Give the location of every parasitized RBC.
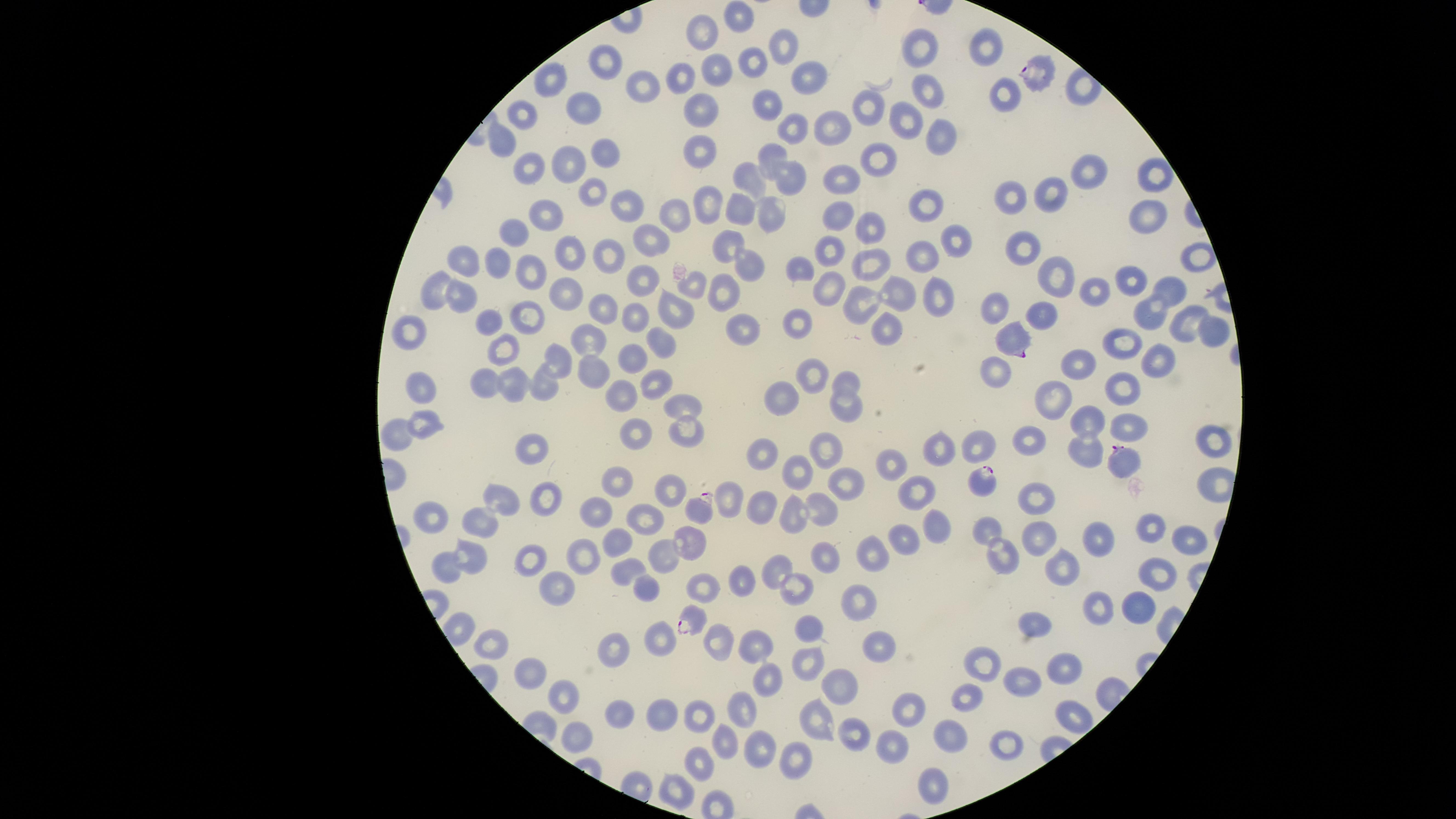

Approximate marker points as {x, y} in pixels.
Parasitized RBCs: {1035, 69}, {1015, 334}, {1123, 460}, {979, 476}, {699, 508}, {693, 619}.

Approximate marker points as {x, y} in pixels. Uninfected RBCs: {737, 18}, {703, 34}, {779, 46}, {923, 48}, {987, 48}, {604, 62}, {750, 67}, {717, 69}, {685, 77}, {547, 78}, {808, 78}, {644, 86}, {928, 88}, {1003, 97}, {765, 105}, {584, 107}, {868, 108}, {703, 109}, {520, 117}, {907, 118}, {792, 127}, {834, 129}, {941, 133}, {506, 142}, {698, 146}, {606, 149}, {775, 157}, {883, 159}, {574, 164}, {529, 168}, {1090, 173}, {1151, 174}, {793, 175}, {748, 178}, {841, 181}, {592, 190}, {1052, 190}, {1011, 200}, {711, 204}, {930, 204}, {628, 206}, {742, 212}, {835, 213}, {549, 214}, {678, 216}, {771, 216}, {1148, 216}, {517, 225}, {868, 227}, {650, 237}, {953, 238}, {727, 244}, {829, 250}, {1021, 250}, {922, 254}, {569, 256}, {607, 257}, {1197, 257}, {468, 260}, {743, 261}, {870, 261}, {502, 264}, {530, 271}, {798, 272}, {1056, 272}, {1128, 278}, {640, 281}, {691, 285}, {726, 289}, {826, 291}, {1168, 291}, {438, 292}, {567, 292}, {901, 292}, {1094, 292}, {938, 296}, {462, 299}, {860, 301}, {597, 306}, {996, 308}, {680, 310}, {1150, 314}, {632, 315}, {529, 317}, {1043, 319}, {886, 321}, {487, 323}, {799, 323}, {1180, 324}, {743, 327}, {413, 330}, {1209, 331}, {589, 337}, {663, 337}, {1120, 343}, {507, 350}, {558, 358}, {635, 360}, {1079, 362}, {1161, 363}, {593, 370}, {994, 375}, {810, 376}, {661, 384}, {848, 384}, {490, 385}, {544, 385}, {1121, 386}, {419, 387}, {522, 387}, {625, 391}, {1056, 396}, {781, 397}, {847, 404}, {691, 409}, {1089, 419}, {425, 425}, {1132, 425}, {633, 427}, {401, 432}, {684, 433}, {1212, 437}, {1032, 440}, {981, 441}, {538, 445}, {826, 447}, {943, 447}, {1082, 448}, {767, 453}, {893, 463}, {796, 468}, {616, 484}, {847, 485}, {667, 488}, {916, 494}, {544, 497}, {1037, 497}, {501, 498}, {729, 499}, {760, 503}, {824, 508}, {599, 510}, {431, 517}, {644, 517}, {789, 517}, {484, 525}, {936, 525}, {991, 527}, {1149, 528}, {1038, 535}, {903, 537}, {619, 540}, {691, 540}, {1186, 540}, {1098, 544}, {663, 553}, {873, 554}, {586, 555}, {998, 557}, {473, 558}, {830, 559}, {532, 560}, {449, 562}, {1064, 563}, {778, 566}, {630, 568}, {1155, 569}, {741, 580}, {558, 583}, {799, 584}, {648, 589}, {857, 590}, {1098, 605}, {1141, 607}, {1038, 621}, {465, 624}, {806, 624}, {657, 640}, {879, 641}, {491, 642}, {613, 646}, {758, 648}, {808, 661}, {991, 662}, {1063, 667}, {533, 672}, {766, 678}, {1019, 679}, {969, 686}, {841, 687}, {570, 698}, {741, 711}, {622, 712}, {914, 712}, {662, 713}, {701, 715}, {817, 718}, {954, 731}, {854, 732}, {582, 736}, {1008, 744}, {723, 745}, {759, 746}, {890, 751}, {797, 756}, {700, 766}, {932, 781}, {677, 793}. Giemsa stain. Species: Plasmodium falciparum. Thin smear of blood. The visible region is circular. Image is 1456×819 pixels. One field of view of the specimen. Smartphone photograph through the microscope eyepiece.